Classify this cell by malaria status.
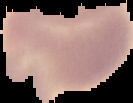

Uninfected.

Summary:
  - Preparation: thin blood smear
  - Image size: 133×103 pixels
  - Image type: segmented cell region on a black background